Give the position of every Plasmodium parasite.
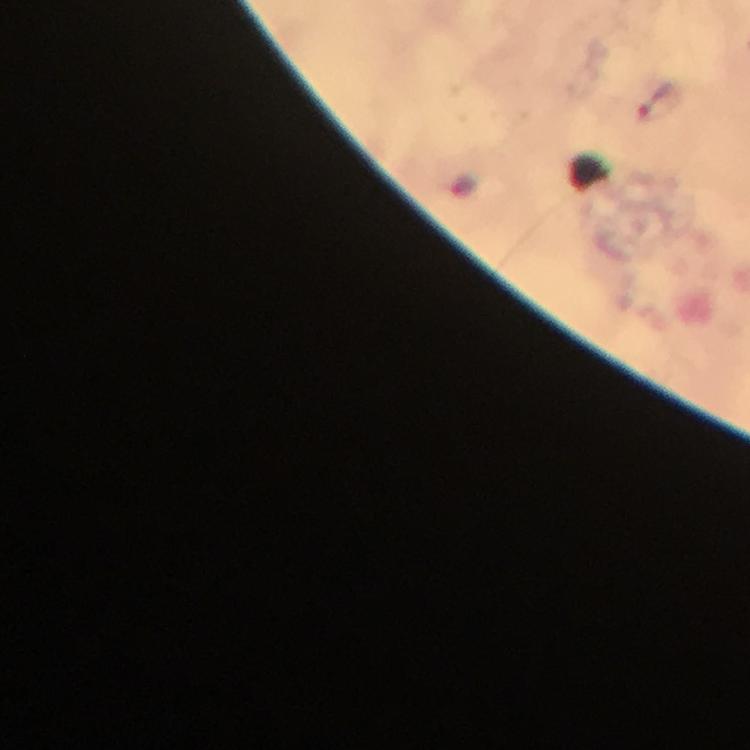

Approximate object centers, in pixels from the top-left corner.
Plasmodium parasites: (x=661, y=100).

From a diagnostic examination for malaria. Immersion oil was used. Cropped region of a single field of view. At 100x magnification. Image is 750×750 pixels. Thick blood film. Giemsa-stained preparation. Photographed through the microscope with a smartphone camera.